Report the malaria status of this cell.
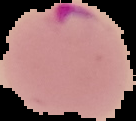

It is parasitized.

preparation = thin blood smear
image type = segmented cell region on a black background
image size = 136×121 pixels